Assess this cell for malaria.
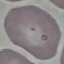
Uninfected.

Thin blood smear. Giemsa stain. Cell patch, automatically extracted from a larger field of view and resized to 64 × 64 pixels. Photographed with a smartphone camera at the microscope eyepiece.